Locate every blood parasite and identify its species.
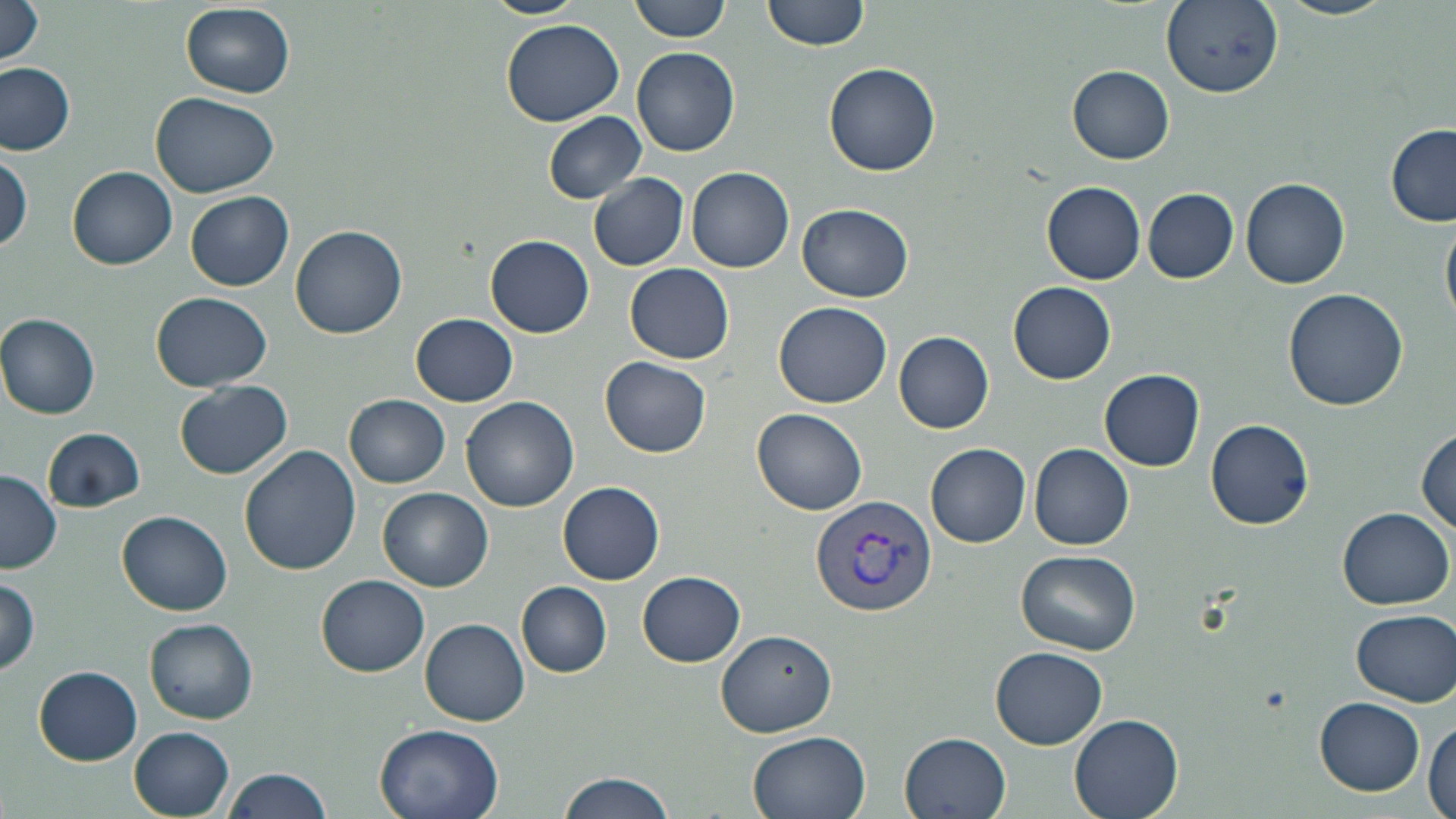

Approximate bounding boxes as (x1,y1)-(x2,y2) corner pairs in pixels.
Plasmodium vivax-infected red blood cells: (809,495)-(938,616).
No Plasmodium falciparum, Plasmodium ovale, Plasmodium malariae, Babesia divergens, or Trypanosoma brucei observed.

slide_level_diagnosis: Plasmodium vivax
magnification: 1000x
preparation: thin blood film
uninfected_red_blood_cell_locations: 'approximate bounding boxes as (x1,y1)-(x2,y2) corner pairs in pixels: (483,0)-(583,18), (629,0)-(732,42), (763,0)-(868,52), (1275,0)-(1397,21), (1,1)-(48,69), (1162,2)-(1284,99), (180,4)-(295,99), (501,20)-(624,125), (633,46)-(740,157), (0,61)-(76,156), (824,63)-(941,177), (1067,66)-(1175,164), (151,93)-(277,196), (543,110)-(646,204), (1386,126)-(1456,226), (0,150)-(30,255), (68,164)-(178,269), (687,166)-(796,273), (589,173)-(688,270), (1241,176)-(1352,289), (1042,183)-(1147,284), (1144,188)-(1238,282), (186,191)-(294,290), (790,204)-(906,404), (798,204)-(915,303), (1441,212)-(1456,332), (291,225)-(407,339), (486,235)-(595,338), (626,263)-(734,364), (1008,280)-(1116,384), (1282,286)-(1409,412), (150,293)-(274,392), (774,300)-(892,406), (0,313)-(102,419), (411,313)-(518,407), (893,330)-(995,433), (600,356)-(712,458), (1100,369)-(1204,470), (175,381)-(293,479), (344,394)-(449,487), (462,397)-(578,510), (753,406)-(868,515), (1205,419)-(1316,530), (44,427)-(145,513), (1415,428)-(1454,539), (927,442)-(1031,547), (1028,442)-(1134,550), (239,444)-(361,575), (0,469)-(62,574), (557,480)-(665,585), (379,487)-(493,592), (348,500)-(479,643), (1336,506)-(1454,609), (119,510)-(233,614), (1017,548)-(1141,654), (637,571)-(746,667), (318,574)-(430,675), (0,576)-(41,677), (517,581)-(611,677), (1350,608)-(1456,706), (421,617)-(530,725), (146,620)-(258,724), (716,630)-(838,738), (990,646)-(1108,749), (35,666)-(141,763), (1315,698)-(1425,793), (1068,713)-(1184,819), (1425,718)-(1455,819), (373,723)-(504,819), (129,728)-(235,817), (745,729)-(874,819), (899,731)-(1010,818), (221,767)-(332,819), (556,771)-(676,819)'
field_of_view: single
stain: May-Grünwald-Giemsa
image_size: 1456×819 pixels
modality: optical microscopy